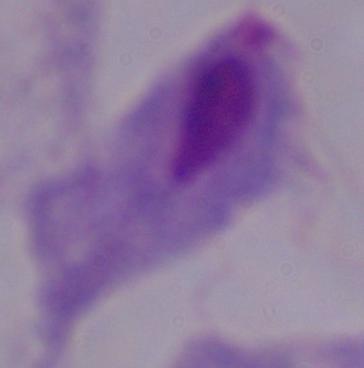

Summary:
  - Identification: trichomonad
  - Modality: photomicrograph
  - Magnification: 1000x